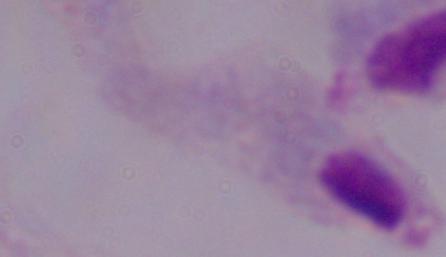
modality = photomicrograph
identification = trichomonad
magnification = 1000x